Outline each blood parasite and name the species.
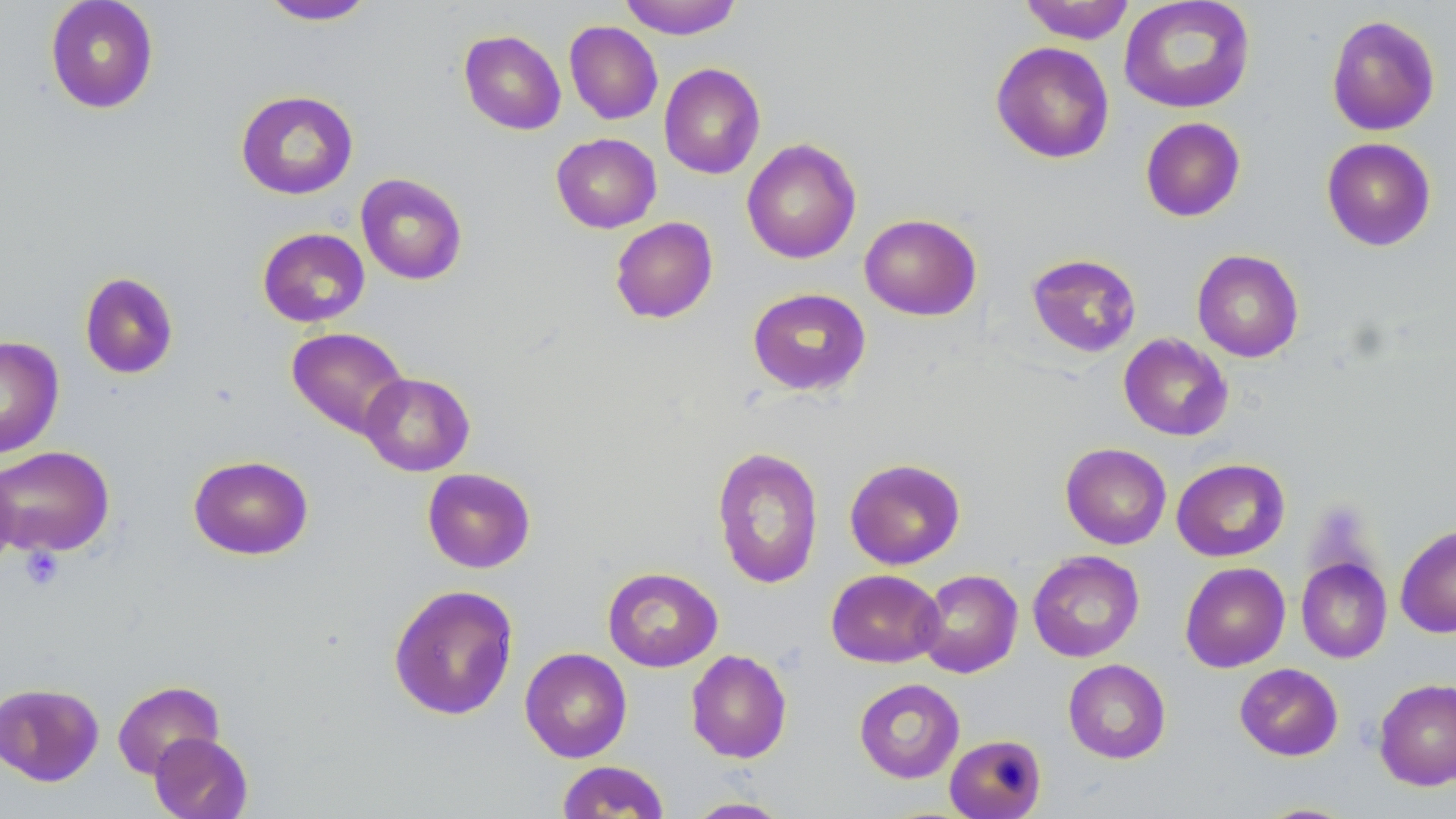

No blood parasites seen.

Approximate bounding boxes as (x1, y1, x2, y2) in pixels. Platelet locations: (21, 546, 64, 591). Uninfected red blood cell locations: (44, 0, 160, 114), (619, 0, 742, 39), (1018, 0, 1135, 44), (1118, 0, 1256, 114), (258, 1, 377, 25), (1325, 14, 1441, 136), (564, 21, 663, 124), (459, 29, 566, 135), (990, 41, 1115, 164), (659, 63, 766, 180), (235, 89, 358, 200), (1140, 117, 1246, 222), (551, 133, 662, 233), (1321, 137, 1437, 251), (741, 138, 862, 264), (355, 173, 468, 285), (859, 213, 982, 321), (610, 217, 718, 324), (257, 227, 370, 327), (1192, 249, 1304, 362), (1026, 253, 1141, 358), (79, 271, 179, 379), (747, 287, 871, 396), (286, 327, 410, 439), (1118, 333, 1233, 441), (0, 336, 65, 459), (359, 372, 474, 476), (1060, 443, 1172, 549), (0, 445, 115, 556), (712, 446, 824, 589), (187, 455, 314, 560), (844, 458, 966, 570), (1172, 458, 1290, 562), (0, 461, 18, 576), (422, 468, 536, 573), (1395, 524, 1456, 638), (1027, 550, 1145, 662), (1296, 557, 1392, 663), (1180, 562, 1290, 672), (602, 567, 723, 672), (826, 569, 944, 668), (916, 569, 1023, 678), (388, 584, 519, 721), (519, 647, 632, 763), (686, 649, 792, 763), (1063, 659, 1171, 763), (1234, 663, 1343, 761), (853, 678, 965, 783), (1373, 678, 1456, 791), (112, 680, 224, 779), (0, 682, 104, 786), (149, 731, 253, 819), (945, 733, 1047, 819), (556, 760, 669, 818), (683, 796, 793, 818), (1250, 802, 1361, 818). Slide-level diagnosis: negative for blood parasites. Single field of view. Optical microscopy. Image is 1456×819 pixels. Captured at 1000x magnification. Thin blood film. May-Grünwald-Giemsa-stained preparation.